Report the malaria status of this cell.
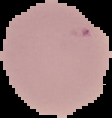
It is uninfected.

Summary:
  - Preparation: thin blood smear
  - Image size: 112×118 pixels
  - Image type: cell region segmented out of the field of view; surrounding area masked to black